Name the blood parasite species.
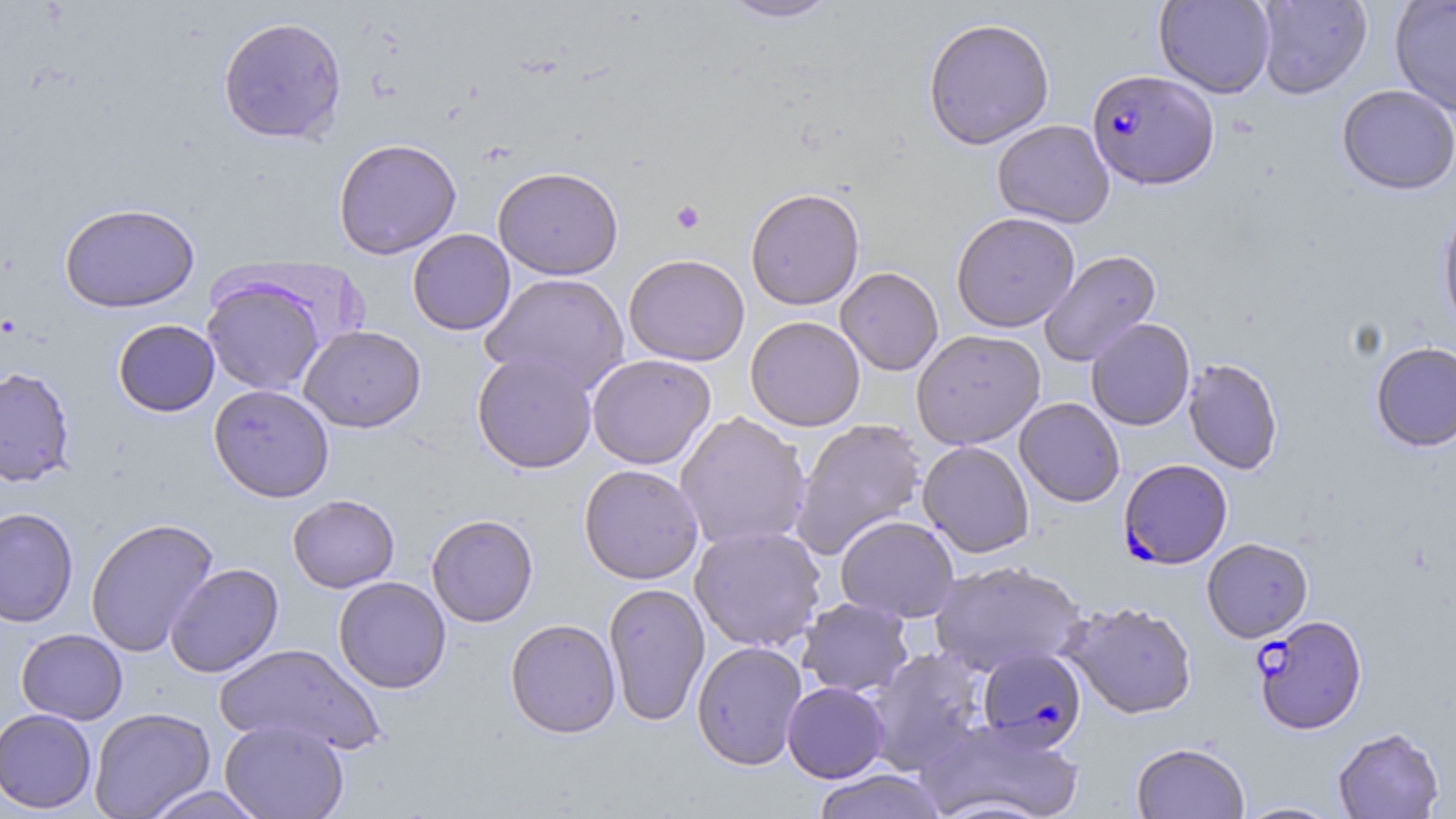
Plasmodium falciparum.

Summary:
  - Coordinate format: approximate bounding boxes as (x1, y1, x2, y2) in pixels
  - Platelet locations: (670, 200, 705, 234)
  - Plasmodium falciparum-infected red blood cell locations: (1086, 69, 1219, 190), (1119, 458, 1232, 569), (1252, 615, 1368, 735), (977, 647, 1086, 750)
  - Uninfected red blood cell locations: (720, 0, 841, 23), (1154, 0, 1275, 98), (1255, 0, 1372, 99), (1390, 0, 1456, 117), (217, 16, 347, 145), (922, 17, 1055, 150), (1336, 85, 1456, 196), (992, 119, 1115, 228), (332, 138, 462, 260), (493, 166, 624, 280), (745, 187, 865, 310), (1437, 201, 1456, 341), (59, 202, 200, 313), (951, 212, 1080, 332), (407, 229, 516, 335), (1039, 250, 1162, 367), (623, 254, 750, 366), (835, 267, 944, 376), (481, 272, 631, 394), (201, 275, 328, 397), (745, 315, 866, 432), (1086, 318, 1195, 431), (113, 319, 220, 416), (299, 325, 426, 432), (911, 329, 1046, 450), (1370, 341, 1456, 452), (471, 351, 597, 473), (587, 354, 716, 469), (1182, 357, 1284, 475), (0, 366, 76, 487), (208, 383, 335, 502), (1014, 398, 1125, 507), (675, 411, 812, 552), (790, 418, 927, 560), (917, 441, 1035, 558), (578, 464, 704, 585), (287, 493, 400, 593), (0, 506, 79, 628), (426, 513, 539, 627), (835, 515, 960, 623), (85, 517, 219, 657), (689, 525, 827, 652), (1201, 538, 1313, 642), (928, 560, 1087, 677), (165, 562, 284, 678), (333, 576, 451, 694), (603, 582, 710, 726), (796, 597, 914, 698), (1061, 601, 1198, 720), (505, 618, 621, 738), (16, 628, 128, 724), (214, 641, 386, 756), (691, 641, 808, 770), (864, 647, 987, 775), (782, 682, 890, 783), (88, 706, 215, 819), (0, 708, 97, 813), (917, 717, 1086, 819), (220, 719, 349, 819), (1333, 728, 1445, 819), (1131, 742, 1249, 819), (812, 769, 948, 819), (140, 785, 270, 818), (1234, 801, 1343, 818)
  - Preparation: thin blood film
  - Image size: 1456×819 pixels
  - Modality: optical microscopy
  - Field of view: single
  - Stain: May-Grünwald-Giemsa
  - Magnification: 1000x